Evaluate for Plasmodium parasites.
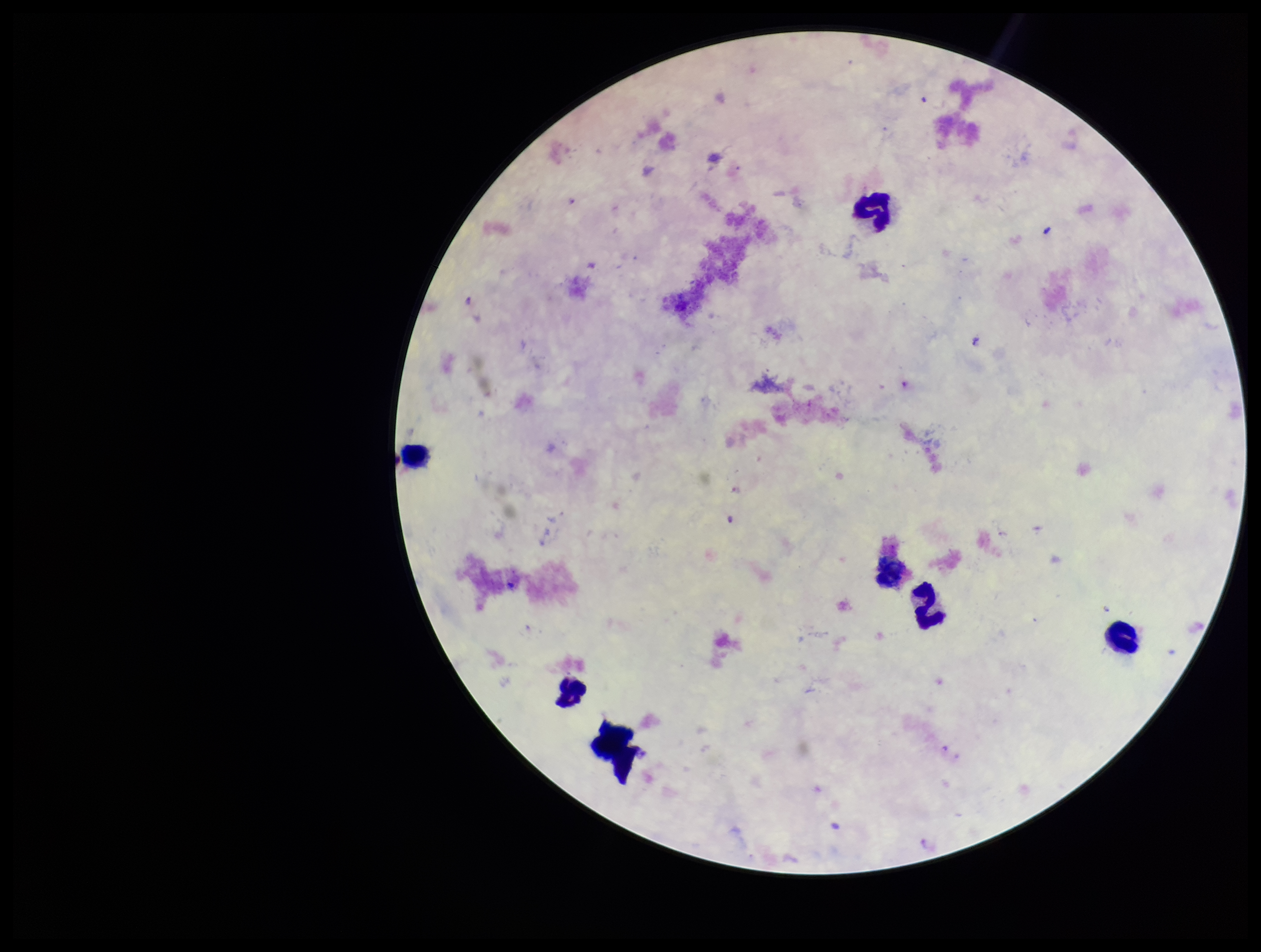
None seen.

{
  "preparation": "thick",
  "capture": "smartphone photograph through the microscope eyepiece",
  "image_size": "1261×952 pixels",
  "species_reported_for_this_patient": "Plasmodium falciparum",
  "leukocyte_count": 7,
  "parasite_count": 0,
  "field_of_view": "single",
  "patient_malaria_status": "positive",
  "stain": "Giemsa"
}